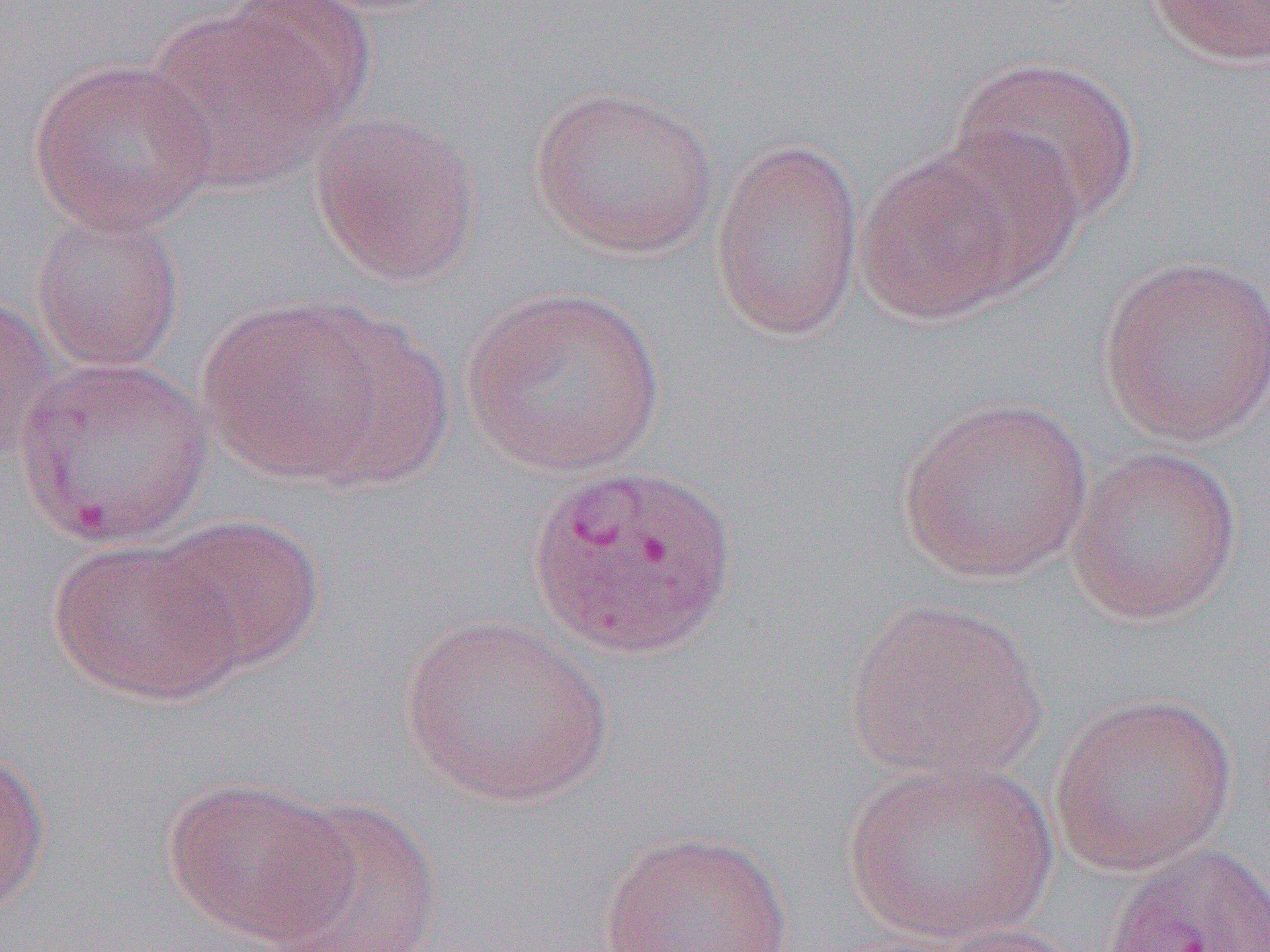
Approximate bounding boxes as named x1/y1/x2/y2 corners in pixels. Uninfected red blood cell locations: (x1=209, y1=0, x2=374, y2=144), (x1=1140, y1=0, x2=1270, y2=68), (x1=145, y1=9, x2=341, y2=189), (x1=949, y1=56, x2=1142, y2=225), (x1=28, y1=58, x2=219, y2=235), (x1=528, y1=84, x2=720, y2=259), (x1=309, y1=111, x2=481, y2=287), (x1=920, y1=132, x2=1085, y2=294), (x1=710, y1=136, x2=866, y2=341), (x1=856, y1=148, x2=1032, y2=325), (x1=30, y1=206, x2=186, y2=374), (x1=1097, y1=254, x2=1270, y2=445), (x1=462, y1=284, x2=666, y2=478), (x1=0, y1=289, x2=57, y2=463), (x1=195, y1=294, x2=415, y2=484), (x1=14, y1=356, x2=214, y2=547), (x1=895, y1=396, x2=1094, y2=584), (x1=1065, y1=445, x2=1243, y2=626), (x1=149, y1=513, x2=325, y2=676), (x1=47, y1=537, x2=241, y2=705), (x1=843, y1=597, x2=1050, y2=785), (x1=398, y1=614, x2=612, y2=807), (x1=1048, y1=691, x2=1238, y2=877), (x1=0, y1=739, x2=51, y2=916), (x1=842, y1=757, x2=1057, y2=946), (x1=159, y1=775, x2=355, y2=947), (x1=265, y1=797, x2=445, y2=952), (x1=597, y1=829, x2=795, y2=952), (x1=914, y1=921, x2=1093, y2=952). Slide-level diagnosis: Plasmodium vivax. Thin blood smear. Single field of view. Image is 1270×952 pixels. 1000x magnification. Light microscopy.